State which parasite is depicted.
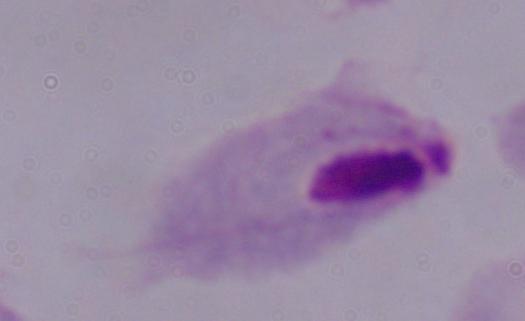
A trichomonad.

modality: photomicrograph
magnification: 1000x